Classify this cell by malaria status.
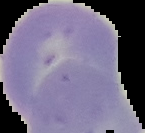

Uninfected.

image type = segmented cell region with the area outside set to black
image size = 145×133 pixels
preparation = thin blood smear